Locate every Plasmodium parasite.
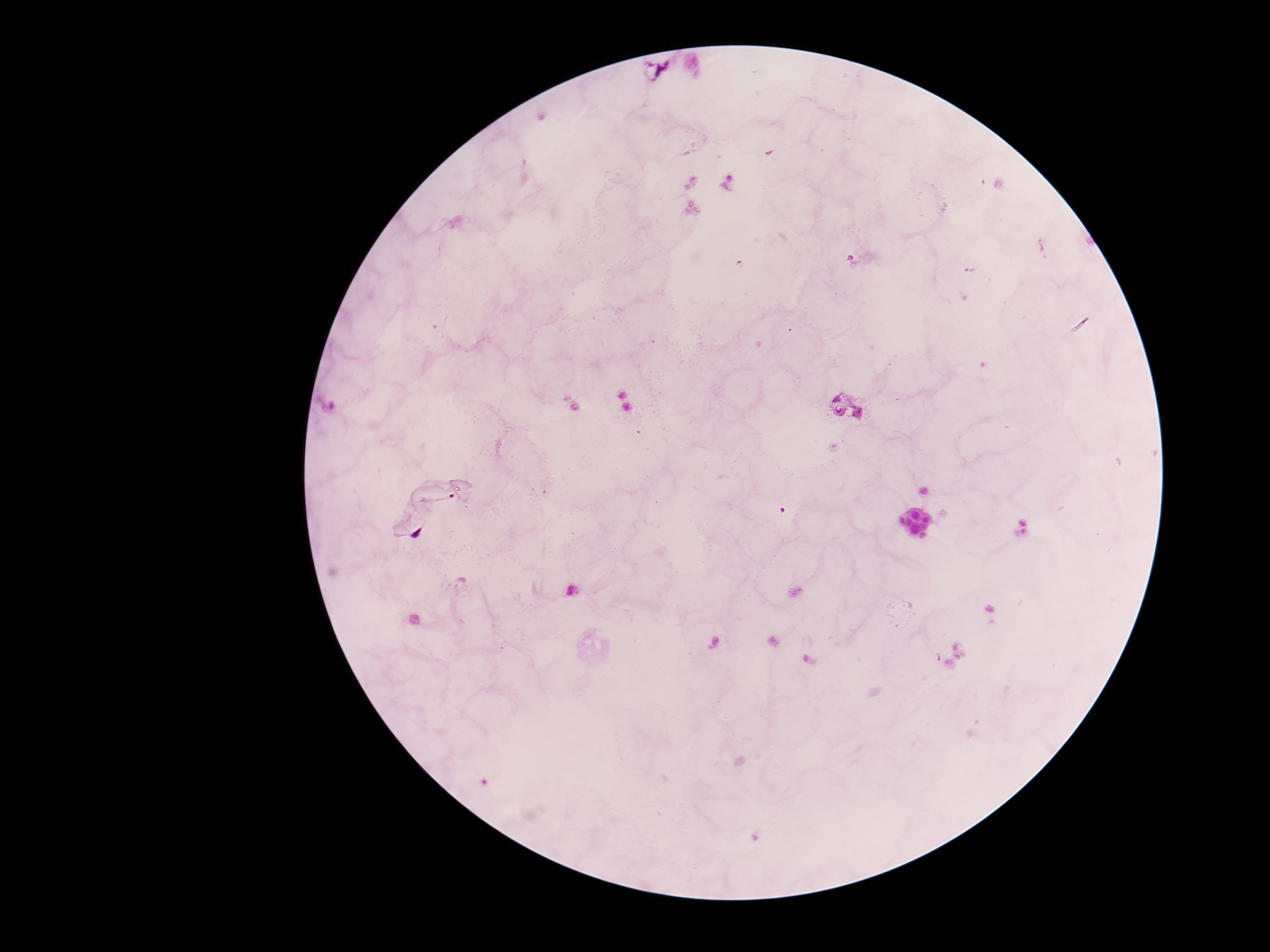
Approximate centers as (x, y) in pixels.
Plasmodium parasites: (667, 69), (847, 408), (426, 513).

Summary:
  - Capture: smartphone camera through the microscope eyepiece
  - Stain: Giemsa
  - Magnification: 100x
  - Preparation: thick peripheral-blood smear
  - Field of view: one from this slide
  - Image size: 1270×952 pixels
  - Patient malaria status: infected